Locate every Plasmodium parasite.
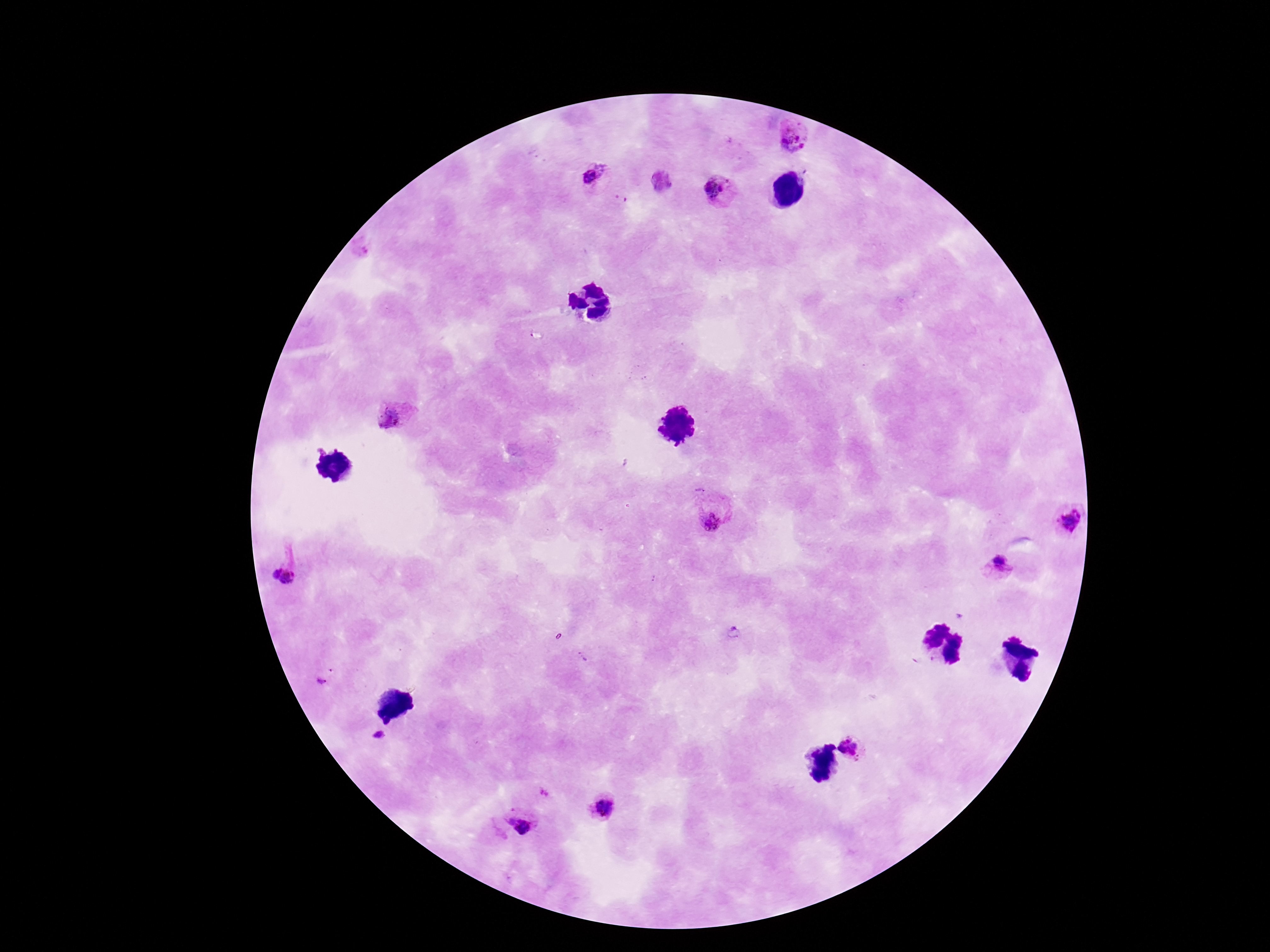

Approximate centers as [x, y] in pixels.
Plasmodium parasites: [795, 135], [590, 175], [718, 188], [394, 417], [715, 514], [1068, 520], [999, 565], [273, 572], [290, 579], [321, 681], [379, 735], [853, 749], [603, 808], [521, 824].

Summary:
  - Stain: Giemsa
  - Capture: smartphone camera through the microscope eyepiece
  - Patient malaria status: infected
  - Preparation: thick peripheral-blood smear
  - Image size: 1270×952 pixels
  - Field of view: one from this slide
  - Magnification: 100x